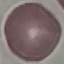
malaria status = uninfected
preparation = thin blood film
image type = cell patch, automatically extracted from a larger field of view and resized to 64 × 64 pixels
capture = smartphone camera at the microscope eyepiece
stain = Giemsa